State the preparation type.
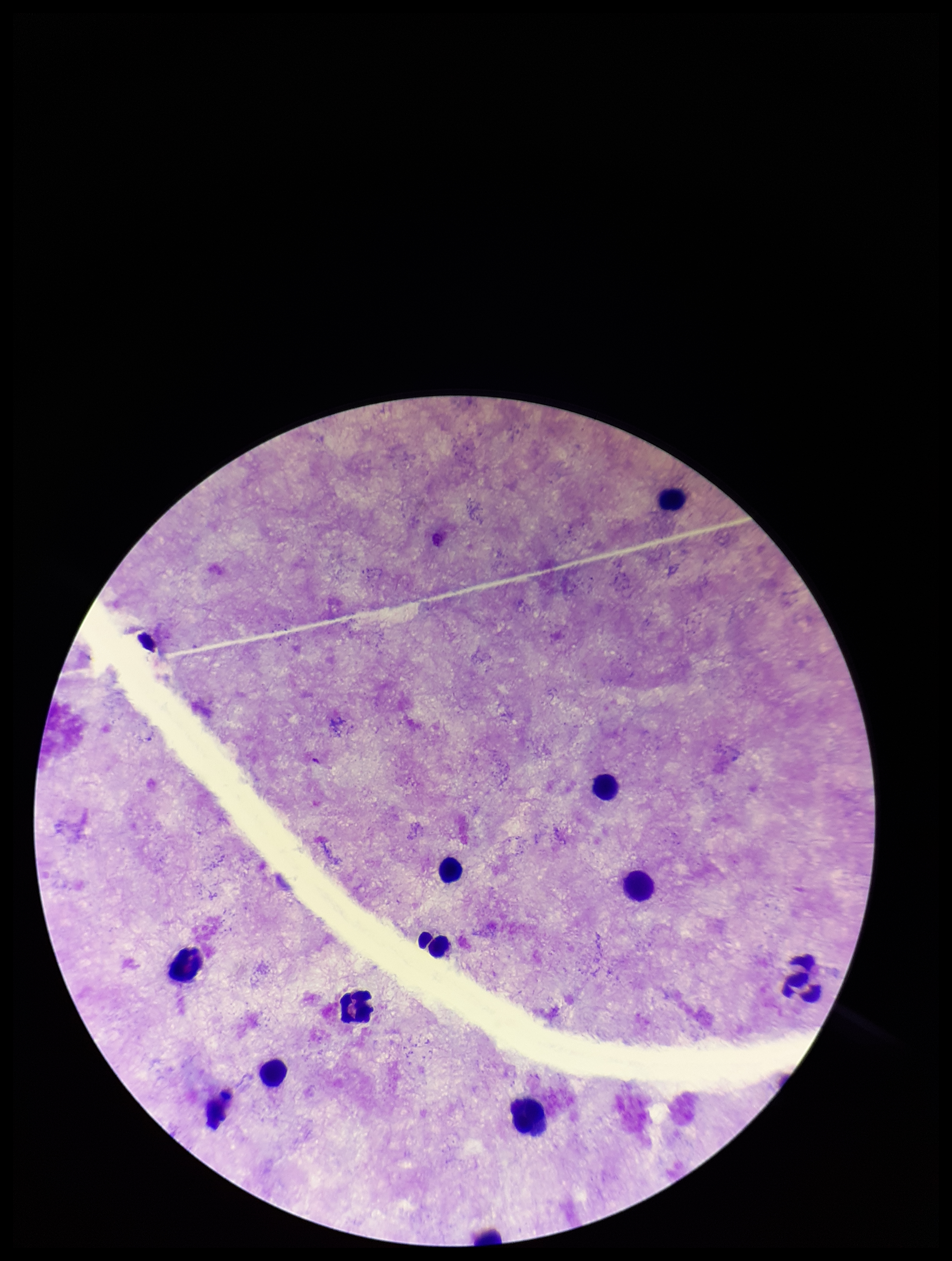
A thick smear.

Summary:
  - Patient malaria status: negative
  - Field of view: single
  - Capture: smartphone photograph through the microscope eyepiece
  - Leukocyte count: 12
  - Parasite count: 0
  - Image size: 952×1261 pixels
  - Stain: Giemsa
  - Plasmodium parasites: none detected